Locate every Plasmodium ovale-infected red blood cell.
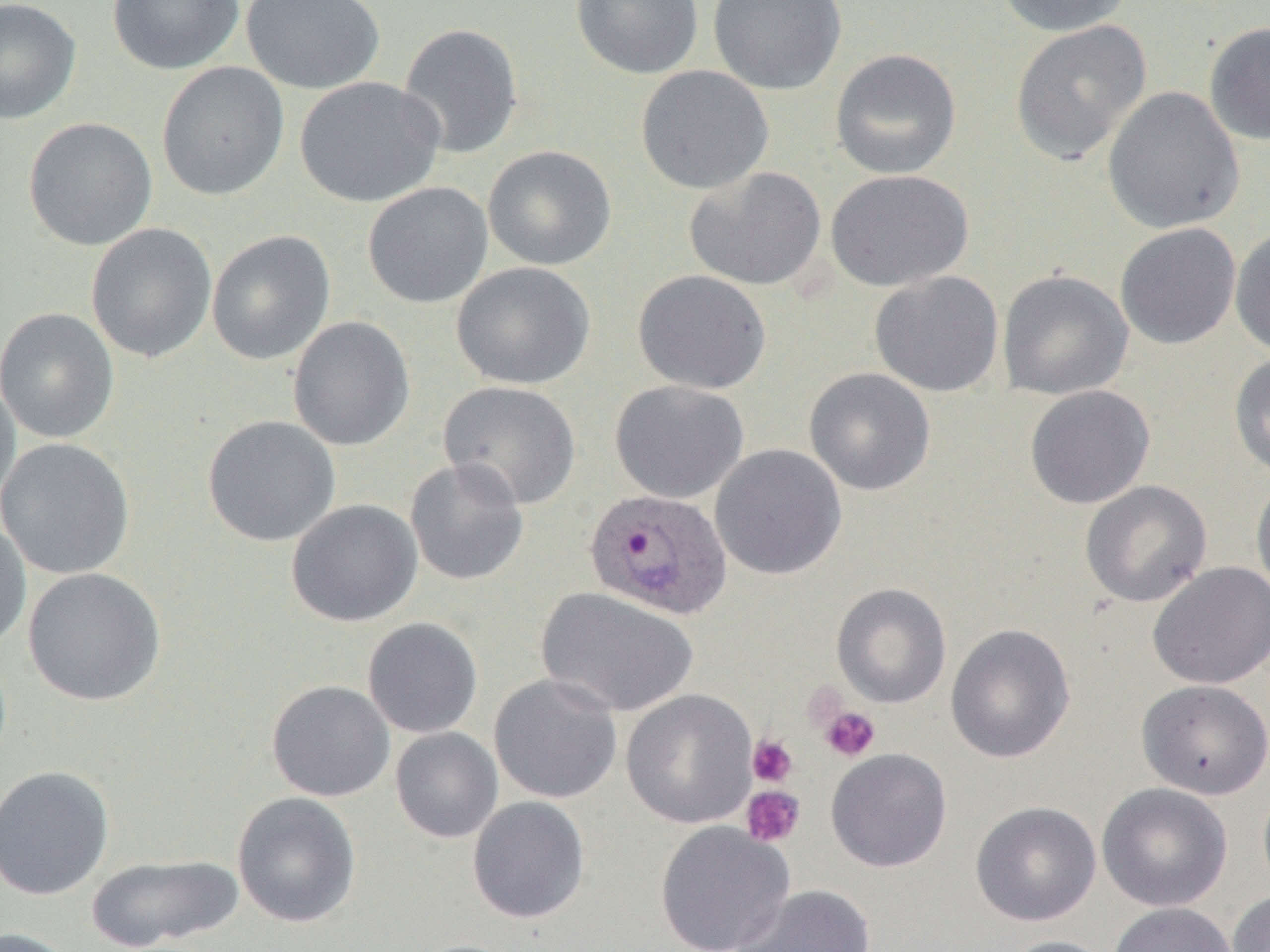
Approximate bounding boxes as named x1/y1/x2/y2 corners in pixels.
Plasmodium ovale-infected red blood cells: (x1=584, y1=487, x2=733, y2=620).

Summary:
  - Uninfected red blood cell locations: (x1=0, y1=0, x2=81, y2=124), (x1=107, y1=0, x2=246, y2=75), (x1=240, y1=0, x2=386, y2=94), (x1=570, y1=0, x2=704, y2=80), (x1=707, y1=0, x2=847, y2=95), (x1=994, y1=0, x2=1135, y2=37), (x1=1010, y1=20, x2=1151, y2=164), (x1=1203, y1=21, x2=1270, y2=146), (x1=397, y1=23, x2=524, y2=159), (x1=829, y1=48, x2=962, y2=179), (x1=156, y1=62, x2=289, y2=201), (x1=635, y1=65, x2=774, y2=194), (x1=294, y1=76, x2=445, y2=208), (x1=1102, y1=86, x2=1245, y2=234), (x1=23, y1=117, x2=158, y2=251), (x1=483, y1=145, x2=617, y2=271), (x1=684, y1=167, x2=827, y2=291), (x1=825, y1=169, x2=974, y2=292), (x1=362, y1=182, x2=493, y2=309), (x1=85, y1=223, x2=218, y2=363), (x1=1115, y1=223, x2=1241, y2=350), (x1=1230, y1=226, x2=1270, y2=358), (x1=206, y1=230, x2=336, y2=365), (x1=451, y1=262, x2=596, y2=390), (x1=632, y1=269, x2=772, y2=395), (x1=997, y1=269, x2=1134, y2=400), (x1=869, y1=271, x2=1004, y2=397), (x1=0, y1=308, x2=119, y2=443), (x1=287, y1=316, x2=415, y2=451), (x1=1229, y1=352, x2=1270, y2=481), (x1=804, y1=367, x2=936, y2=496), (x1=0, y1=374, x2=20, y2=510), (x1=438, y1=380, x2=582, y2=510), (x1=609, y1=380, x2=749, y2=504), (x1=1024, y1=385, x2=1155, y2=509), (x1=202, y1=415, x2=341, y2=547), (x1=0, y1=437, x2=135, y2=580), (x1=709, y1=444, x2=847, y2=580), (x1=404, y1=456, x2=529, y2=586), (x1=1251, y1=475, x2=1270, y2=603), (x1=1079, y1=480, x2=1213, y2=607), (x1=286, y1=499, x2=423, y2=627), (x1=0, y1=518, x2=32, y2=652), (x1=1147, y1=562, x2=1270, y2=690), (x1=22, y1=567, x2=166, y2=706), (x1=831, y1=583, x2=952, y2=709), (x1=535, y1=586, x2=699, y2=718), (x1=362, y1=617, x2=483, y2=738), (x1=946, y1=623, x2=1075, y2=763), (x1=489, y1=673, x2=623, y2=804), (x1=1136, y1=679, x2=1270, y2=799), (x1=266, y1=680, x2=395, y2=802), (x1=621, y1=688, x2=758, y2=829), (x1=390, y1=727, x2=503, y2=843), (x1=826, y1=748, x2=952, y2=872), (x1=0, y1=765, x2=115, y2=901), (x1=1096, y1=782, x2=1232, y2=911), (x1=232, y1=792, x2=361, y2=928), (x1=467, y1=796, x2=591, y2=923), (x1=970, y1=801, x2=1101, y2=926), (x1=654, y1=820, x2=795, y2=952), (x1=86, y1=853, x2=243, y2=951), (x1=728, y1=884, x2=876, y2=952), (x1=1227, y1=889, x2=1270, y2=952), (x1=1107, y1=902, x2=1237, y2=952), (x1=0, y1=927, x2=76, y2=952), (x1=997, y1=936, x2=1115, y2=952)
  - Platelet locations: (x1=820, y1=706, x2=881, y2=762), (x1=747, y1=735, x2=798, y2=787), (x1=740, y1=785, x2=805, y2=848)
  - Slide-level diagnosis: Plasmodium ovale
  - Magnification: 1000x
  - Image size: 1270×952 pixels
  - Field of view: one of a larger specimen
  - Preparation: thin blood film
  - Modality: optical microscopy